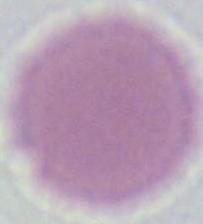
Summary:
  - Modality: micrograph
  - Magnification: 1000x
  - Identification: erythrocyte